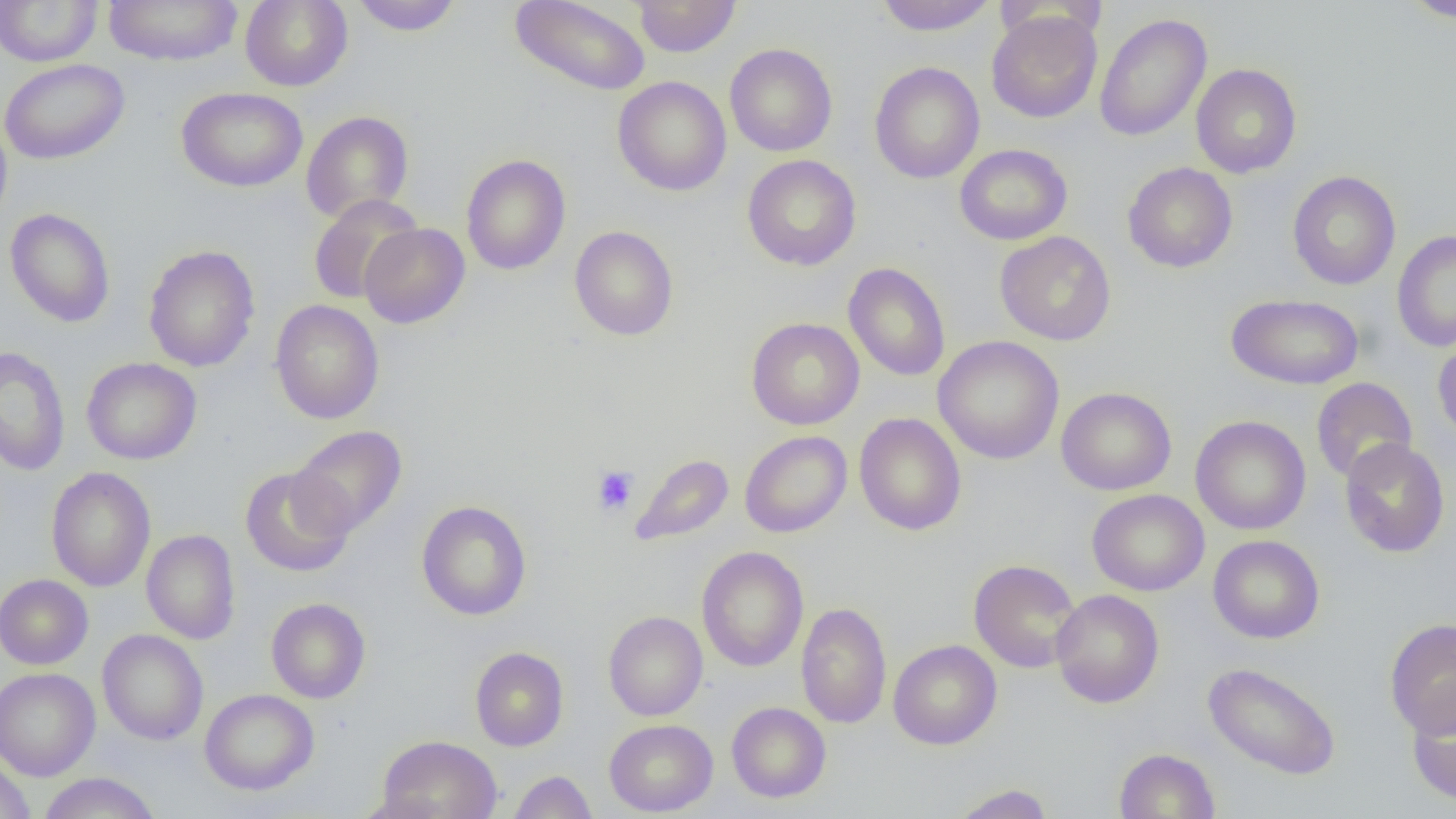
Summary:
  - Coordinate format: approximate bounding boxes as (x1,y1)-(x2,y2) corner pairs in pixels
  - Platelet locations: (592,466)-(639,516)
  - Uninfected red blood cell locations: (0,0)-(103,67), (102,0)-(242,67), (239,0)-(353,91), (351,0)-(463,36), (510,0)-(651,96), (632,0)-(742,57), (875,0)-(997,36), (1400,0)-(1456,22), (987,10)-(1102,123), (1094,13)-(1212,142), (725,43)-(837,157), (0,58)-(130,165), (869,61)-(985,184), (1190,63)-(1302,178), (613,76)-(731,196), (176,86)-(308,192), (301,110)-(413,224), (0,115)-(13,230), (954,144)-(1072,245), (461,154)-(571,275), (741,154)-(861,271), (1122,161)-(1238,273), (1286,171)-(1401,290), (308,194)-(423,305), (4,208)-(116,328), (359,223)-(470,328), (569,225)-(679,340), (1392,230)-(1456,352), (995,231)-(1116,346), (143,245)-(260,372), (843,263)-(950,381), (1226,293)-(1364,390), (269,299)-(384,424), (746,317)-(864,430), (1432,330)-(1456,447), (933,336)-(1064,464), (0,347)-(70,476), (81,357)-(202,465), (1311,377)-(1417,483), (1056,386)-(1176,495), (854,413)-(967,536), (1190,415)-(1311,535), (290,425)-(407,537), (740,430)-(852,537), (1339,438)-(1450,558), (630,454)-(734,547), (240,466)-(354,578), (46,467)-(156,591), (1087,489)-(1209,596), (416,500)-(531,621), (141,529)-(240,645), (1208,535)-(1325,644), (696,546)-(809,672), (968,559)-(1082,673), (0,574)-(93,670), (1050,589)-(1164,708), (266,598)-(371,703), (795,602)-(892,728), (603,611)-(708,720), (1385,617)-(1456,738), (97,629)-(209,745), (888,640)-(1002,750), (470,647)-(569,751), (1202,661)-(1341,780), (0,667)-(100,781), (199,688)-(319,795), (1406,690)-(1456,808), (726,702)-(831,802), (604,719)-(718,816), (377,735)-(502,819), (1114,748)-(1220,819), (0,758)-(34,819), (508,770)-(597,819), (37,772)-(161,819), (948,783)-(1055,819), (351,792)-(450,819)
  - Slide-level diagnosis: negative for blood parasites
  - Modality: optical microscopy
  - Image size: 1456×819 pixels
  - Preparation: thin blood smear
  - Magnification: 1000x
  - Field of view: one of a larger specimen